Locate and identify every blood parasite.
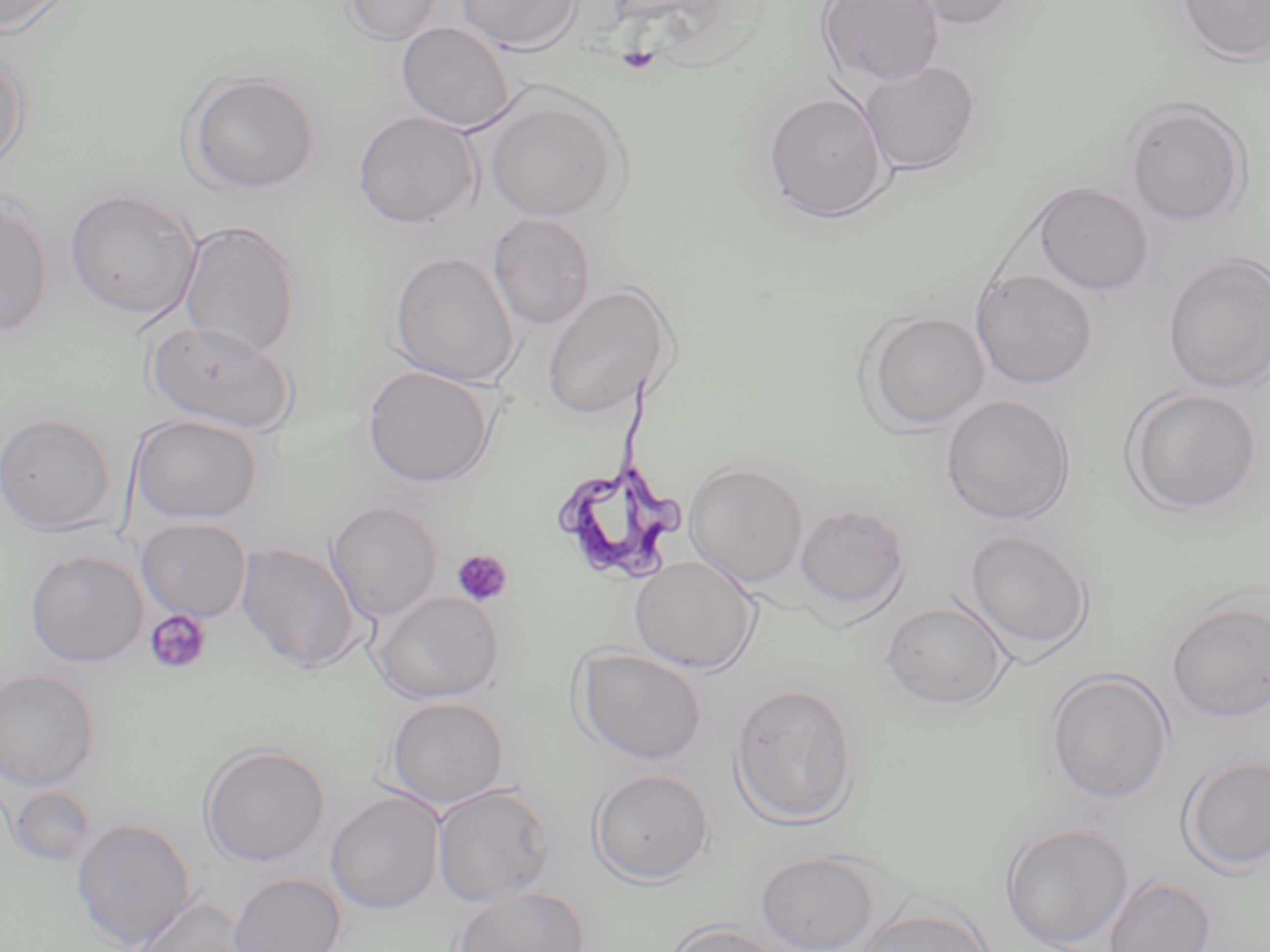

Approximate bounding boxes as (x1, y1, x2, y2) in pixels.
Trypanosoma brucei: (557, 368, 687, 585).
No Plasmodium falciparum, Plasmodium ovale, Plasmodium malariae, Plasmodium vivax, or Babesia divergens observed.

slide-level diagnosis = Trypanosoma brucei
modality = optical microscopy
image size = 1270×952 pixels
preparation = thin blood smear
uninfected red blood cell locations = approximate bounding boxes as (x1, y1, x2, y2) in pixels: (0, 0, 76, 36), (340, 0, 446, 44), (454, 0, 584, 54), (817, 0, 947, 88), (897, 0, 1024, 31), (1173, 0, 1270, 66), (396, 21, 518, 132), (0, 47, 32, 172), (859, 61, 983, 176), (181, 70, 321, 195), (762, 89, 893, 224), (485, 93, 625, 224), (1121, 95, 1253, 227), (351, 110, 482, 230), (1032, 181, 1154, 296), (64, 187, 202, 322), (0, 194, 54, 338), (487, 212, 597, 331), (178, 220, 302, 359), (388, 251, 520, 388), (1161, 252, 1270, 395), (969, 268, 1099, 391), (540, 283, 676, 422), (857, 310, 992, 432), (147, 318, 296, 435), (362, 365, 498, 488), (1121, 386, 1264, 515), (939, 395, 1076, 525), (0, 411, 117, 534), (130, 414, 264, 524), (683, 462, 809, 588), (326, 500, 444, 622), (794, 501, 911, 620), (137, 517, 252, 622), (962, 529, 1094, 656), (235, 542, 362, 674), (24, 549, 149, 668), (629, 555, 759, 674), (371, 591, 504, 704), (1165, 596, 1269, 724), (880, 598, 1013, 710), (573, 647, 708, 765), (1044, 668, 1176, 805), (0, 669, 101, 791), (729, 682, 860, 828), (384, 696, 510, 809), (199, 742, 331, 867), (1178, 754, 1270, 876), (588, 768, 716, 886), (430, 783, 558, 906), (6, 784, 98, 868), (325, 791, 444, 914), (70, 817, 197, 950), (1000, 822, 1134, 949), (755, 850, 882, 952), (229, 872, 347, 952), (1103, 874, 1217, 952), (450, 886, 590, 952), (123, 896, 258, 952), (853, 905, 994, 952), (665, 920, 791, 952)
platelet locations = approximate bounding boxes as (x1, y1, x2, y2) in pixels: (616, 47, 661, 75), (451, 549, 513, 607), (145, 609, 213, 675)
field of view = one of a larger specimen
magnification = 1000x
stain = May-Grünwald-Giemsa